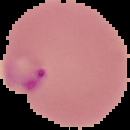
image type = segmented cell region on a black background
preparation = thin blood film
result = Plasmodium parasites identified
image size = 130×130 pixels